Describe the morphology of the red blood cells.
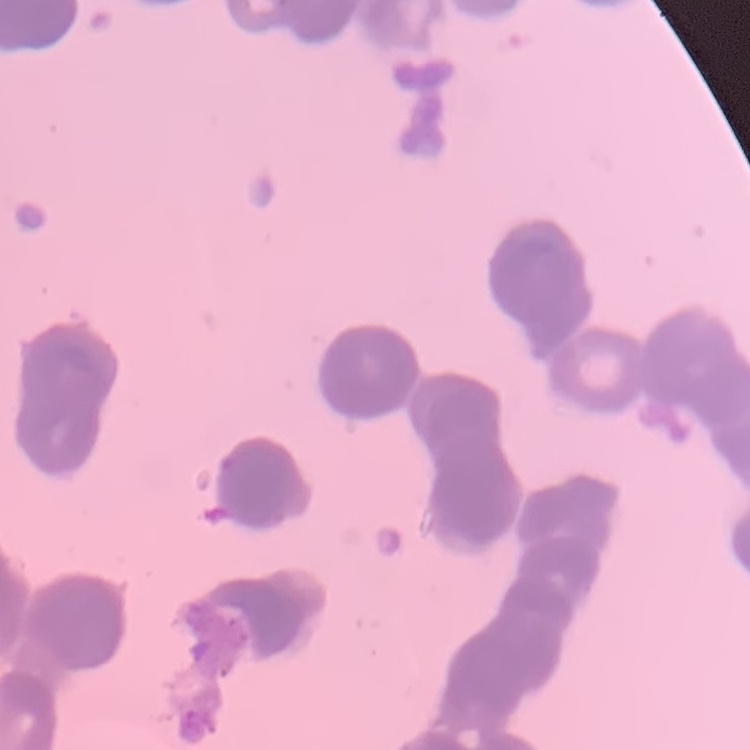

Rouleaux formation.

Summary:
  - Stain: Field's or Giemsa
  - Image type: square crop of a larger photomicrograph
  - Preparation: thin blood smear